Describe the morphology of the erythrocytes.
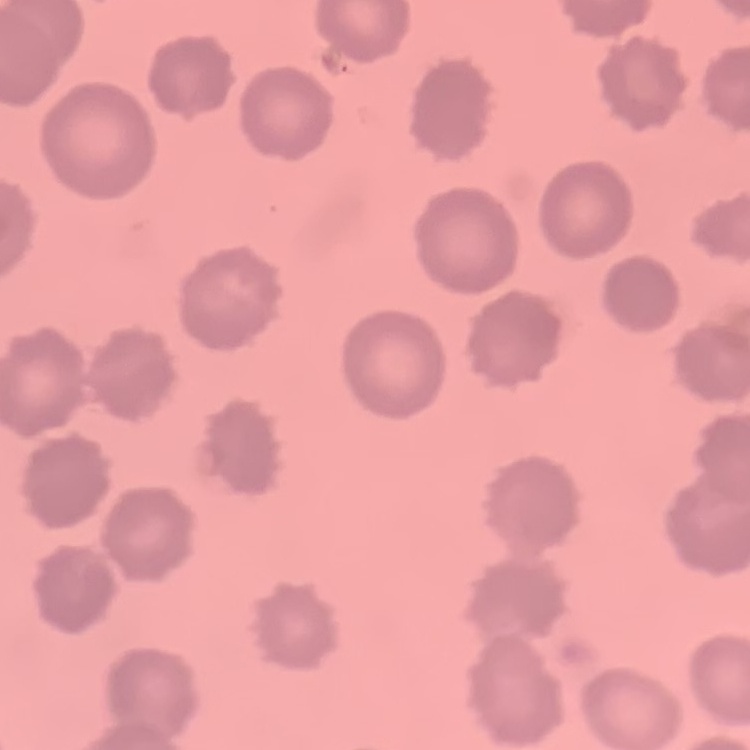
No rouleaux formation.

Summary:
  - Stain: Field's or Giemsa
  - Image type: one tile cut from a larger photomicrograph
  - Preparation: thin blood film